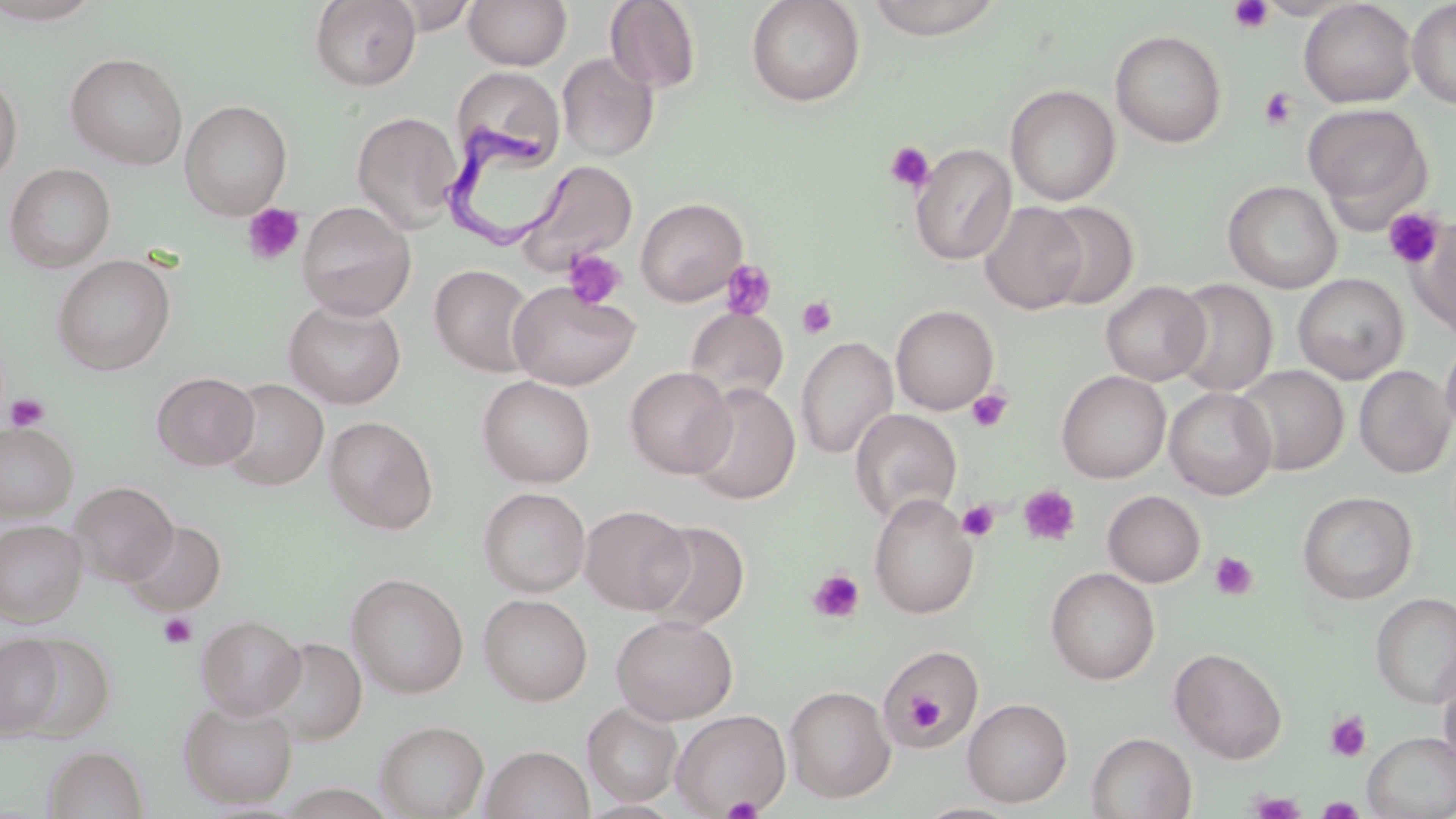

slide_level_diagnosis: Trypanosoma brucei
modality: light microscopy
uninfected_red_blood_cell_locations: 'approximate bounding boxes as [x1, y1, x2, y2] in pixels: [0, 0, 107, 26], [309, 0, 421, 91], [463, 0, 572, 70], [745, 0, 866, 107], [862, 0, 1007, 40], [604, 1, 702, 93], [1299, 1, 1417, 108], [1406, 1, 1456, 109], [1110, 29, 1227, 148], [65, 52, 188, 169], [557, 52, 659, 161], [451, 67, 565, 165], [0, 71, 22, 187], [1005, 84, 1120, 205], [179, 100, 291, 219], [1303, 103, 1432, 221], [351, 112, 462, 231], [910, 143, 1016, 265], [514, 160, 639, 275], [4, 163, 115, 272], [1222, 180, 1342, 293], [635, 198, 747, 306], [296, 201, 417, 320], [1037, 201, 1139, 309], [979, 202, 1087, 314], [1411, 217, 1455, 340], [52, 254, 175, 374], [430, 264, 537, 377], [1293, 273, 1409, 384], [1168, 279, 1278, 396], [508, 281, 640, 391], [1101, 281, 1211, 385], [283, 299, 406, 409], [891, 305, 998, 414], [684, 307, 789, 408], [1440, 334, 1456, 440], [796, 336, 897, 459], [1233, 365, 1349, 476], [1354, 365, 1455, 478], [625, 366, 736, 478], [1056, 370, 1171, 483], [152, 371, 259, 470], [478, 375, 595, 487], [220, 378, 328, 490], [688, 384, 800, 505], [1165, 386, 1277, 500], [850, 409, 962, 525], [324, 416, 438, 534], [0, 422, 77, 521], [70, 481, 178, 586], [479, 487, 590, 596], [1104, 491, 1205, 587], [1298, 491, 1417, 603], [868, 493, 979, 619], [580, 505, 694, 614], [124, 519, 226, 614], [0, 520, 86, 626], [641, 520, 750, 631], [1046, 567, 1160, 685], [347, 572, 469, 698], [1371, 591, 1456, 708], [478, 593, 593, 705], [196, 614, 306, 719], [611, 614, 738, 724], [12, 633, 115, 742], [0, 634, 64, 737], [262, 636, 367, 744], [1169, 647, 1288, 763], [877, 648, 982, 753], [1438, 659, 1456, 770], [784, 685, 896, 803], [963, 697, 1073, 807], [178, 699, 298, 809], [583, 703, 683, 807], [670, 709, 791, 816], [375, 720, 489, 819], [1362, 731, 1456, 819], [1086, 732, 1196, 818], [42, 745, 148, 819], [482, 746, 594, 819], [913, 802, 1025, 818]'
platelet_locations: 'approximate bounding boxes as [x1, y1, x2, y2] in pixels: [1228, 0, 1274, 34], [1259, 87, 1298, 130], [884, 141, 935, 194], [243, 203, 304, 265], [1383, 208, 1445, 269], [562, 249, 627, 310], [719, 259, 777, 320], [797, 296, 838, 339], [966, 388, 1014, 433], [5, 393, 49, 431], [1019, 484, 1081, 547], [957, 500, 1000, 541], [1210, 551, 1258, 600], [807, 569, 865, 624], [158, 612, 198, 648], [901, 689, 950, 732], [1325, 711, 1372, 762], [1250, 792, 1304, 818], [721, 794, 764, 819], [1318, 797, 1364, 818]'
field_of_view: one of a larger specimen
preparation: thin blood smear
stain: May-Grünwald-Giemsa
image_size: 1456×819 pixels
trypanosoma_brucei_locations: 'approximate bounding boxes as [x1, y1, x2, y2] in pixels: [445, 128, 583, 251]'
magnification: 1000x